Name the parasite shown.
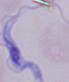

This is a trypanosome.

Captured at 1000x magnification. Micrograph.